Report the malaria status of this cell.
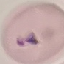
Parasitized.

stain = Giemsa
image type = cell patch, automatically extracted from a larger field of view and resized to 64 × 64 pixels
capture = smartphone camera at the microscope eyepiece
preparation = thin smear